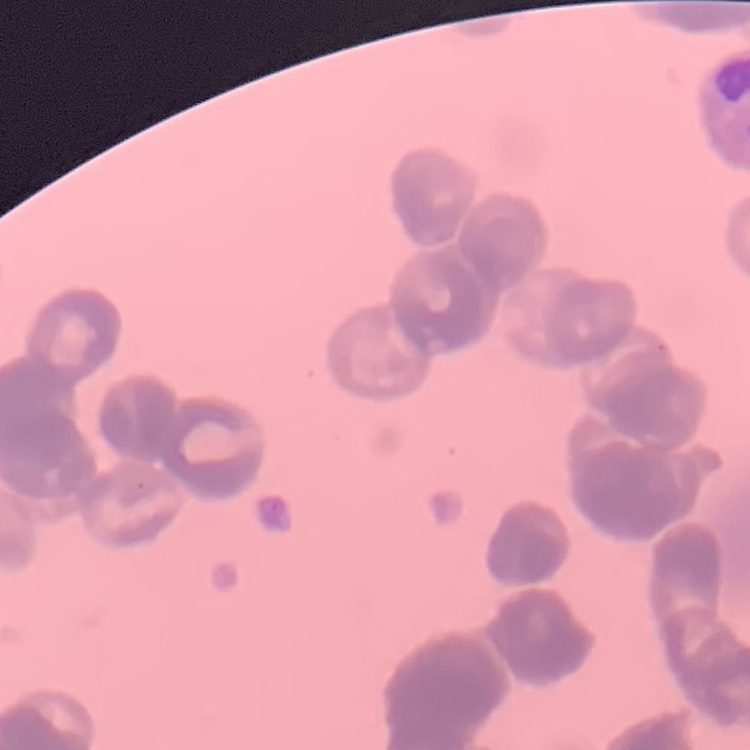

Summary:
  - Erythrocyte morphology: rouleaux formation
  - Stain: Field's or Giemsa
  - Image type: one tile cut from a larger photomicrograph
  - Preparation: thin peripheral smear